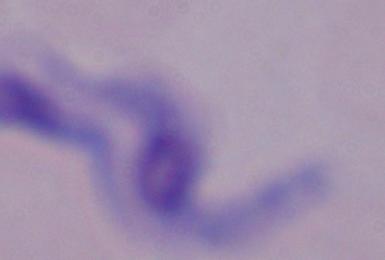

Summary:
  - Modality: photomicrograph
  - Identification: trypanosome
  - Magnification: 1000x